Give the extent of all Plasmodium falciparum-infected red blood cells.
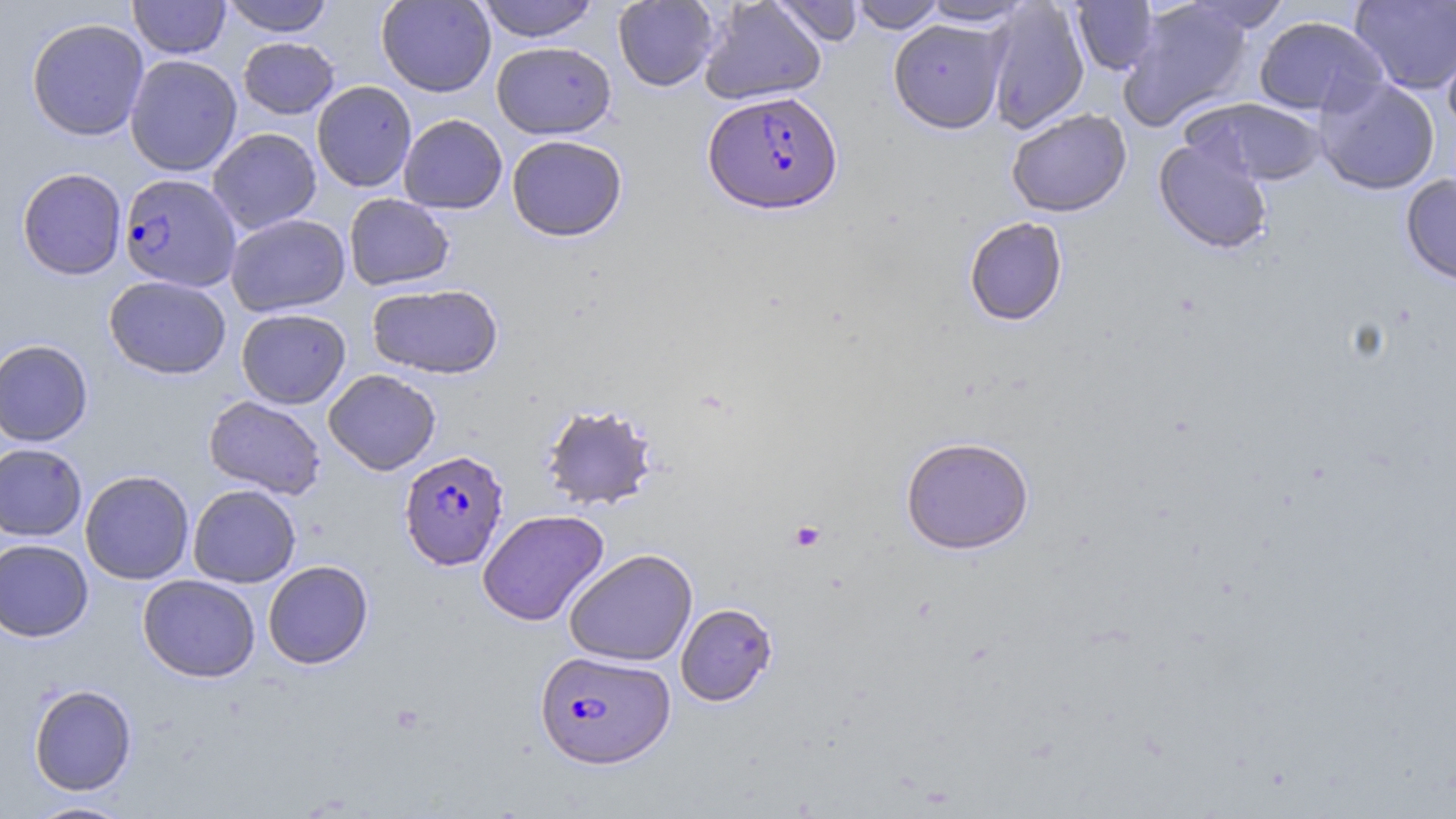
Approximate bounding boxes as (x1,y1)-(x2,y2) corner pairs in pixels.
Plasmodium falciparum-infected red blood cells: (703,90)-(843,215), (119,173)-(241,291), (399,449)-(509,569), (534,650)-(675,768).

slide_level_diagnosis: Plasmodium falciparum
platelet_locations: 'approximate bounding boxes as (x1,y1)-(x2,y2) corner pairs in pixels: (789,520)-(826,552)'
image_size: 1456×819 pixels
stain: May-Grünwald-Giemsa
uninfected_red_blood_cell_locations: 'approximate bounding boxes as (x1,y1)-(x2,y2) corner pairs in pixels: (128,0)-(230,59), (221,0)-(334,36), (376,0)-(496,97), (476,0)-(600,42), (699,0)-(827,105), (769,0)-(864,47), (848,0)-(945,32), (920,0)-(1033,26), (612,1)-(720,91), (984,1)-(1090,134), (1071,1)-(1159,76), (1118,1)-(1254,130), (1181,1)-(1291,34), (1350,1)-(1455,95), (1253,15)-(1388,117), (25,17)-(149,141), (888,18)-(1009,134), (1441,26)-(1456,137), (238,37)-(339,119), (491,41)-(616,139), (124,54)-(242,176), (1314,76)-(1441,195), (311,81)-(417,192), (1187,97)-(1327,185), (1006,108)-(1131,217), (398,114)-(507,214), (207,128)-(322,234), (506,134)-(628,241), (1153,138)-(1273,254), (17,167)-(127,280), (1400,173)-(1456,285), (344,194)-(454,291), (225,213)-(350,317), (964,216)-(1068,326), (104,275)-(231,379), (367,282)-(503,379), (236,308)-(351,409), (0,339)-(93,446), (323,369)-(440,475), (203,395)-(327,500), (539,402)-(660,511), (900,435)-(1034,554), (0,443)-(87,541), (79,470)-(194,585), (188,484)-(301,588), (477,509)-(609,626), (0,539)-(94,641), (564,548)-(698,667), (263,560)-(373,669), (138,574)-(260,682), (675,602)-(778,706), (28,683)-(137,795), (24,799)-(136,818)'
magnification: 1000x
field_of_view: one of a larger specimen
preparation: thin blood smear
modality: light microscopy